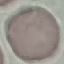 Malaria status: uninfected. Thin blood film. Cell patch, automatically extracted from a larger field of view and resized to 64 × 64 pixels. Acquired by smartphone through the microscope eyepiece. Giemsa stain.